Outline each Plasmodium falciparum-infected red blood cell.
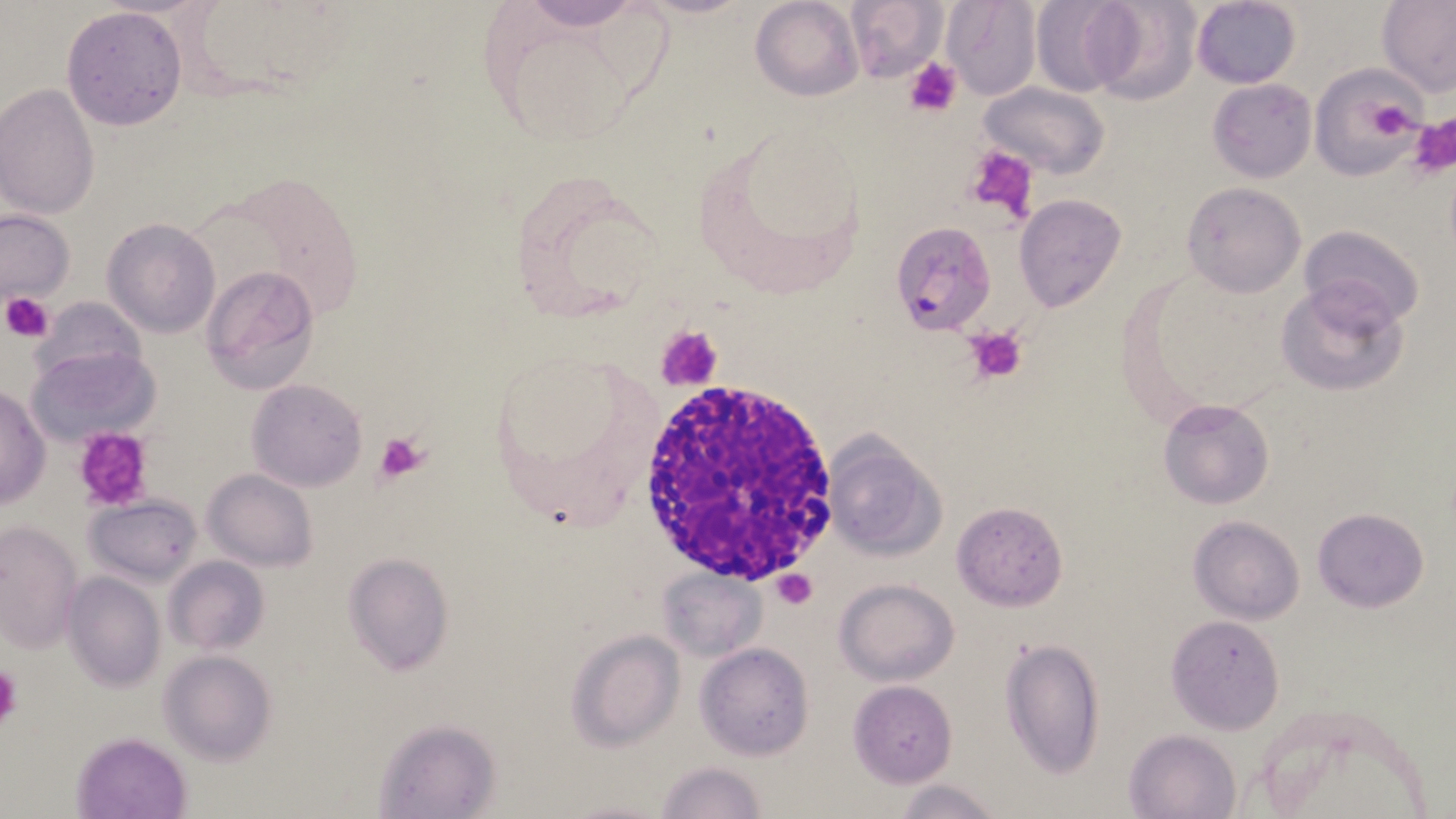
Approximate bounding boxes as (x1,y1)-(x2,y2) corner pairs in pixels.
Plasmodium falciparum-infected red blood cells: (893,227)-(991,335).

Platelet locations: (904,57)-(961,118), (1360,98)-(1417,143), (1411,114)-(1456,176), (961,145)-(1040,223), (4,292)-(55,340), (964,324)-(1029,384), (656,325)-(725,391), (73,428)-(154,511), (374,430)-(432,484), (771,568)-(817,609), (0,663)-(20,728). Uninfected red blood cell locations: (518,0)-(641,30), (750,0)-(863,101), (844,0)-(947,80), (942,0)-(1040,98), (1030,0)-(1135,95), (1083,0)-(1200,105), (1191,0)-(1302,88), (1377,0)-(1456,97), (61,6)-(187,131), (1312,65)-(1426,180), (1208,79)-(1316,183), (979,82)-(1107,179), (0,84)-(100,220), (1180,181)-(1307,299), (1014,194)-(1126,311), (0,210)-(75,305), (101,217)-(220,338), (1300,225)-(1425,332), (201,265)-(320,393), (1275,278)-(1408,397), (33,295)-(146,386), (29,345)-(160,446), (247,378)-(366,490), (0,385)-(49,510), (1158,397)-(1273,509), (821,433)-(945,563), (204,469)-(317,570), (86,494)-(201,586), (952,500)-(1070,610), (1311,506)-(1429,613), (1188,516)-(1305,623), (0,520)-(82,653), (341,552)-(454,676), (163,556)-(269,656), (659,568)-(762,660), (63,571)-(165,692), (835,578)-(958,684), (1168,616)-(1286,738), (1167,617)-(1284,731), (568,629)-(684,750), (1000,639)-(1107,778), (696,641)-(816,761), (158,650)-(276,764), (848,680)-(958,786), (372,717)-(502,819), (1125,728)-(1240,818), (73,732)-(189,817), (653,760)-(766,819), (894,778)-(1004,819). White blood cell locations: (641,372)-(839,586). Slide-level diagnosis: Plasmodium falciparum. May-Grünwald-Giemsa stain. Single field of view. Image is 1456×819 pixels. Thin blood film. Optical microscopy. 1000x magnification.